Comment on the morphology of the erythrocytes.
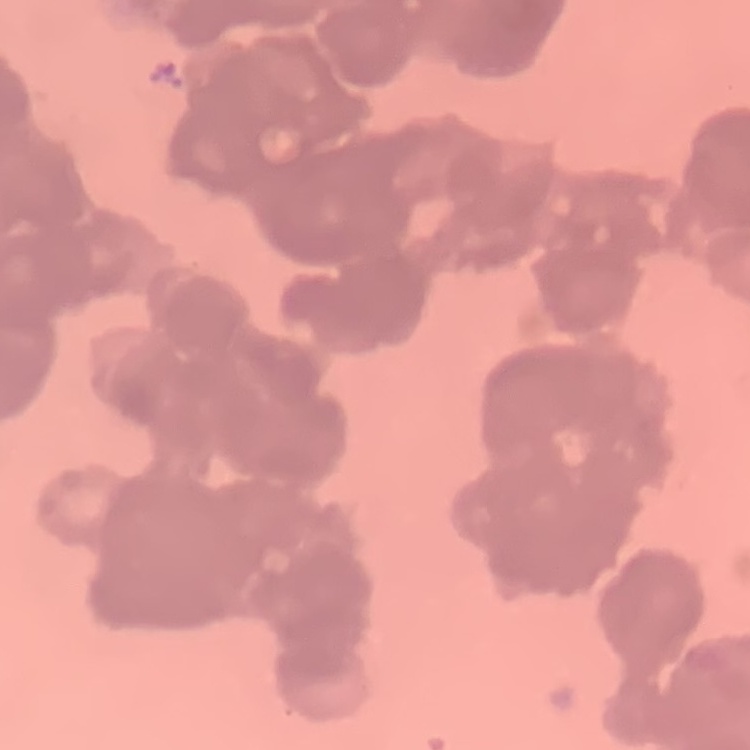

Rouleaux formation.

Field's or Giemsa stain. One tile cut from a larger photomicrograph. Thin peripheral smear.